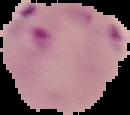
Summary:
  - Result: Plasmodium parasites detected
  - Preparation: thin blood film
  - Image type: segmented cell region with the area outside set to black
  - Image size: 130×115 pixels